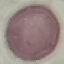
Result: no malaria parasites detected. Giemsa stain. Acquired by smartphone through the microscope eyepiece. Thin blood smear. Automatically extracted cell patch, resized to 64 × 64 pixels.